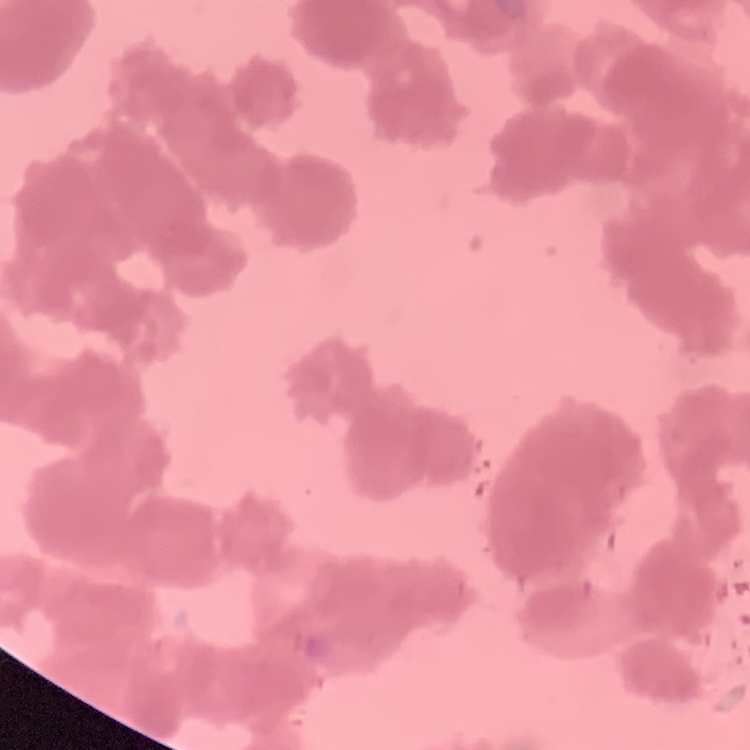

Summary:
  - Erythrocyte morphology: rouleaux formation
  - Preparation: thin blood smear
  - Stain: Field's or Giemsa
  - Image type: square crop of a larger photomicrograph